Assess this cell for malaria.
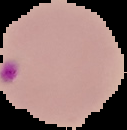

It is parasitized.

The area outside the segmented cell region is set to black. From a thin blood smear. Image is 127×130 pixels.